Report the malaria status of this cell.
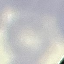

It is uninfected.

Acquired by smartphone through the microscope eyepiece. Cell patch, automatically extracted from a larger field of view and resized to 64 × 64 pixels. Giemsa stain. Thin smear of blood.